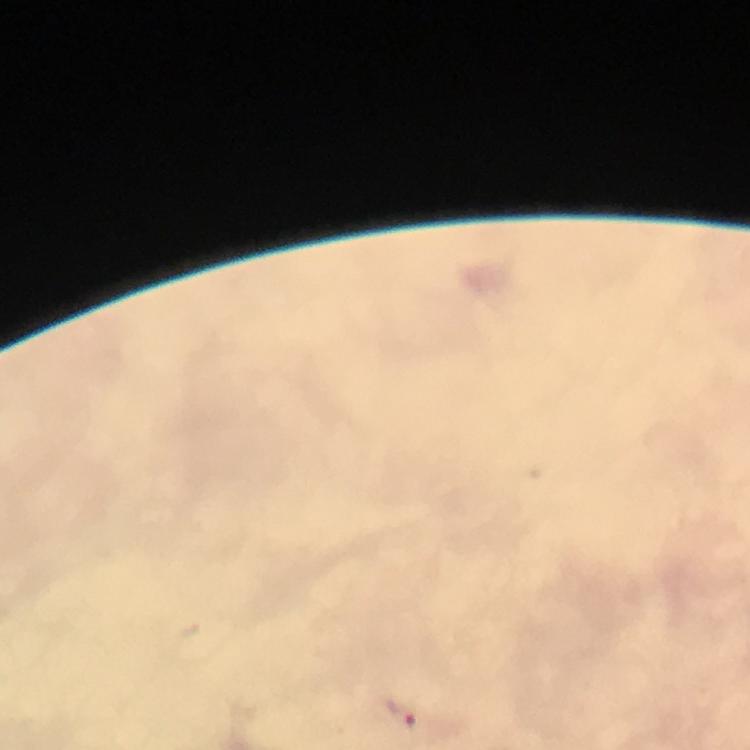

preparation = thick smear
capture = smartphone camera through the microscope
image size = 750×750 pixels
immersion oil = used
cropped from = one field of view
context = from a malaria diagnostic workup
Plasmodium parasite locations = approximate centers as [x, y] in pixels: [403, 715]
stain = Giemsa
magnification = 100x